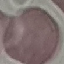
Summary:
  - Malaria status: uninfected
  - Preparation: thin blood film
  - Image type: automatically extracted cell patch, resized to 64 × 64 pixels
  - Capture: smartphone camera at the microscope eyepiece
  - Stain: Giemsa